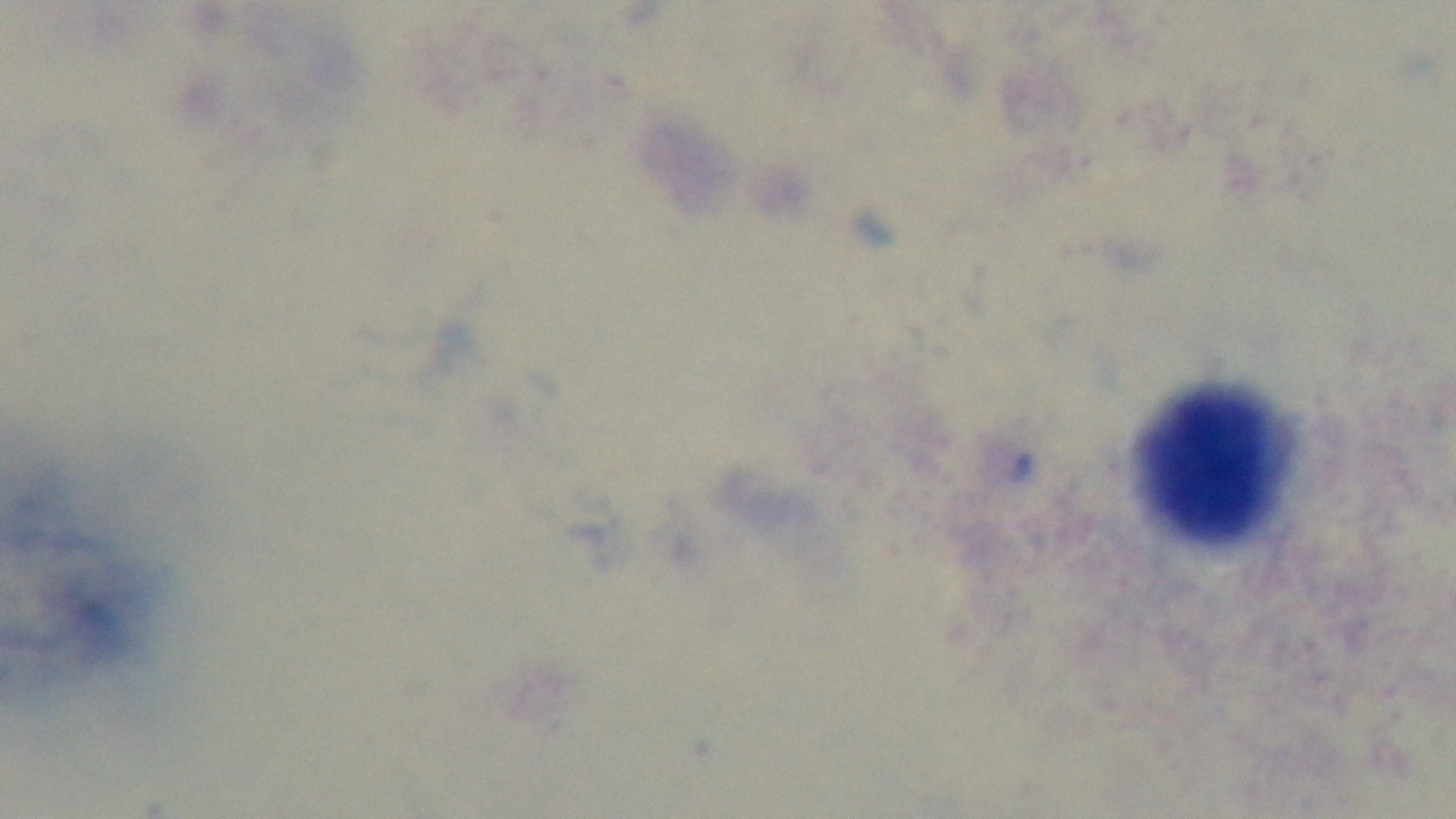

objective = 100x oil immersion
malaria status = negative
capture = mounted 4K digital camera
field of view = single
stain = Giemsa
preparation = thick smear
modality = light microscopy